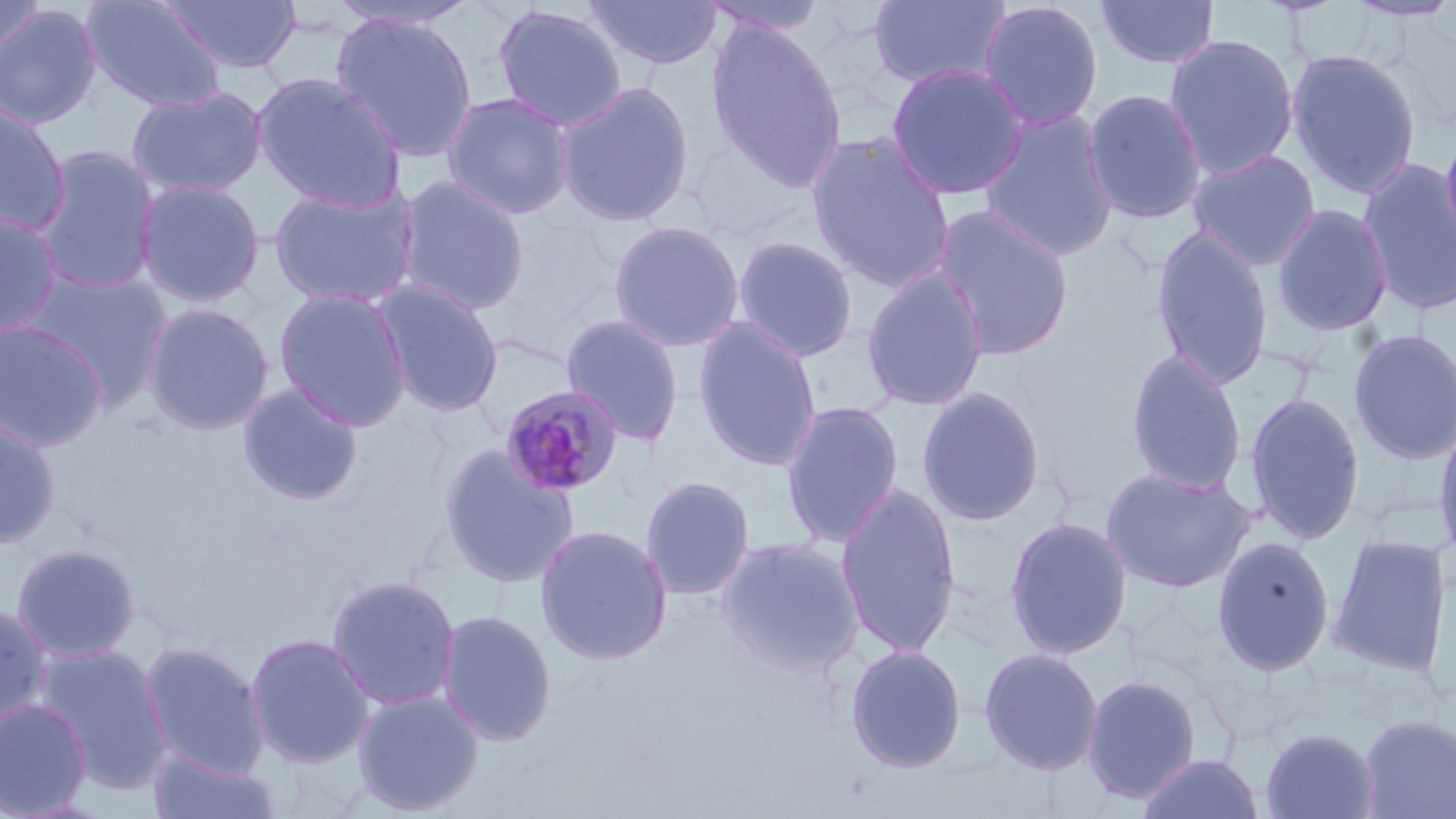
slide_level_diagnosis: Plasmodium malariae
modality: light microscopy
field_of_view: single
stain: May-Grünwald-Giemsa
preparation: thin blood film
image_size: 1456×819 pixels
uninfected_red_blood_cell_locations: 'approximate bounding boxes as (x1, y1, x2, y2) in pixels: (0, 0, 48, 60), (81, 0, 227, 113), (160, 0, 303, 74), (584, 0, 724, 70), (868, 0, 1012, 90), (1095, 0, 1220, 70), (1345, 0, 1456, 23), (327, 1, 481, 33), (700, 1, 829, 36), (976, 1, 1104, 132), (491, 3, 628, 132), (0, 4, 103, 130), (330, 11, 479, 163), (705, 20, 849, 193), (1164, 33, 1300, 180), (1285, 47, 1422, 199), (885, 62, 1028, 201), (252, 73, 407, 211), (555, 81, 696, 227), (125, 85, 268, 198), (1082, 88, 1208, 224), (441, 92, 575, 220), (0, 99, 71, 237), (979, 109, 1120, 261), (4, 111, 118, 268), (1439, 124, 1456, 260), (806, 132, 956, 293), (32, 145, 162, 294), (1188, 149, 1321, 271), (1358, 158, 1456, 315), (394, 174, 531, 316), (134, 178, 266, 307), (268, 184, 420, 310), (931, 203, 1074, 362), (1271, 203, 1394, 336), (0, 210, 64, 339), (607, 220, 745, 353), (1150, 225, 1274, 390), (731, 234, 859, 363), (860, 266, 990, 412), (21, 268, 173, 408), (371, 279, 505, 417), (274, 287, 412, 431), (142, 302, 274, 435), (561, 313, 686, 447), (0, 318, 109, 451), (693, 318, 823, 471), (1348, 328, 1456, 464), (1125, 349, 1248, 495), (237, 382, 364, 506), (916, 386, 1046, 526), (1243, 390, 1365, 545), (780, 399, 904, 548), (0, 415, 61, 548), (1433, 419, 1456, 566), (437, 443, 579, 590), (1100, 466, 1255, 592), (640, 474, 756, 600), (835, 484, 962, 658), (1005, 516, 1132, 660), (534, 523, 673, 665), (1328, 534, 1452, 678), (1211, 535, 1335, 676), (715, 536, 866, 675), (11, 543, 141, 662), (326, 573, 462, 711), (0, 603, 53, 727), (436, 608, 557, 746), (245, 632, 375, 768), (139, 641, 269, 778), (34, 643, 172, 792), (845, 644, 967, 773), (979, 647, 1103, 775), (1081, 674, 1203, 803), (351, 688, 485, 815), (0, 698, 92, 817), (1358, 713, 1456, 818), (1259, 727, 1380, 819), (148, 747, 281, 819), (1135, 751, 1266, 819)'
plasmodium_malariae_infected_red_blood_cell_locations: 'approximate bounding boxes as (x1, y1, x2, y2) in pixels: (499, 384, 624, 498)'
magnification: 1000x